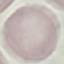
Summary:
  - Malaria status: uninfected
  - Stain: Giemsa
  - Image type: automatically extracted cell patch, resized to 64 × 64 pixels
  - Preparation: thin smear
  - Capture: smartphone through the microscope eyepiece